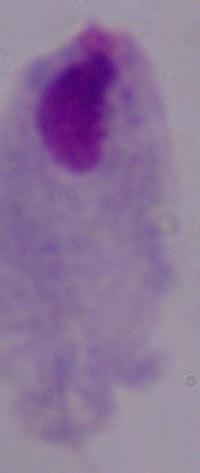 Micrograph. A trichomonad is shown. Captured at 1000x magnification.